Name the blood parasite species.
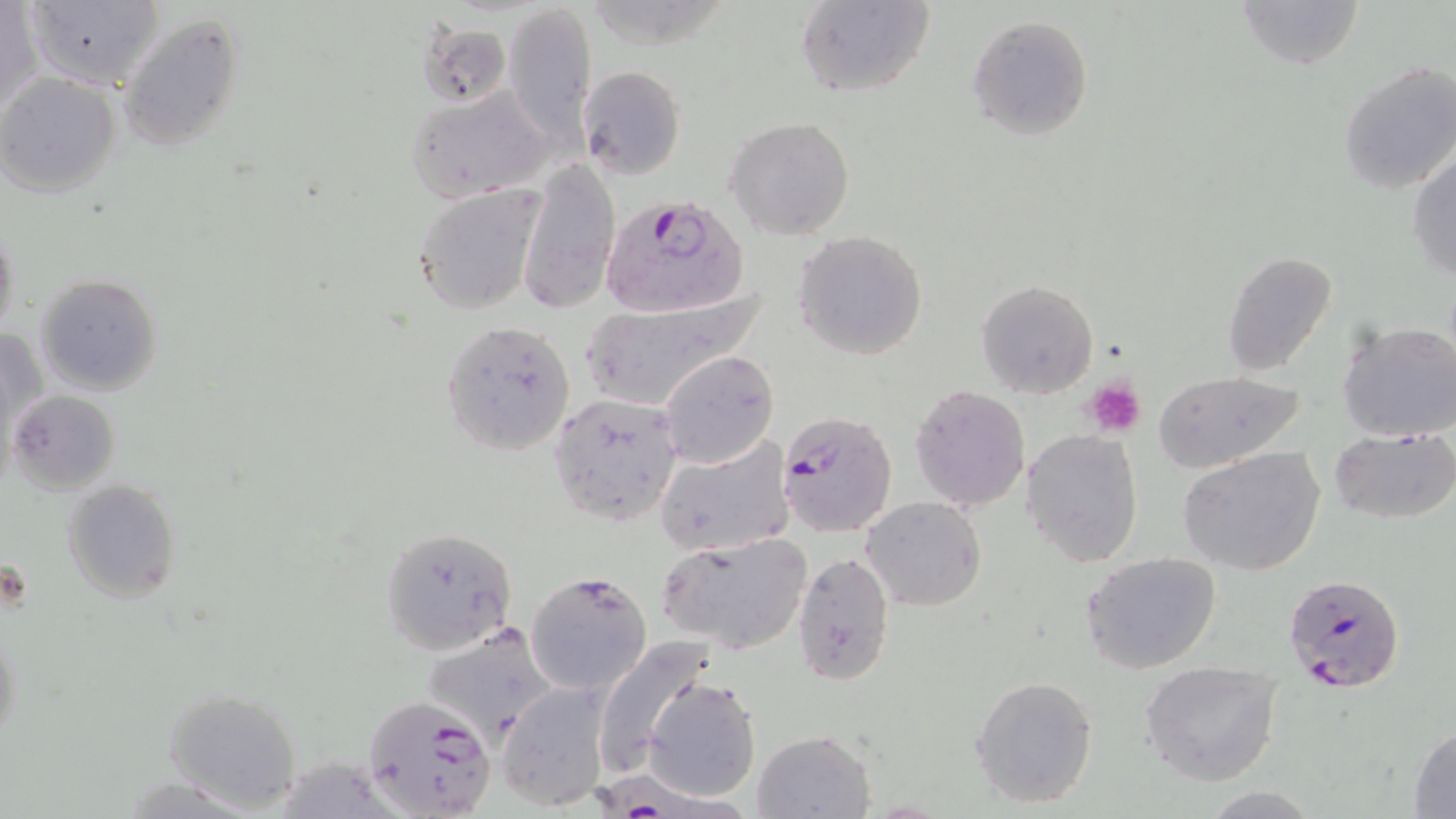
Plasmodium falciparum.

stain = May-Grünwald-Giemsa
Plasmodium falciparum-infected red blood cell locations = approximate bounding boxes as (x1, y1, x2, y2) in pixels: (601, 194, 749, 321), (775, 407, 898, 538), (1282, 572, 1405, 695), (360, 693, 499, 817), (602, 767, 752, 819)
field of view = one of a larger specimen
magnification = 1000x
image size = 1456×819 pixels
platelet locations = approximate bounding boxes as (x1, y1, x2, y2) in pixels: (1084, 378, 1146, 439)
modality = light microscopy
preparation = thin blood film
uninfected red blood cell locations = approximate bounding boxes as (x1, y1, x2, y2) in pixels: (795, 0, 937, 99), (1229, 0, 1363, 70), (1, 1, 41, 118), (23, 1, 163, 89), (503, 4, 597, 140), (117, 13, 247, 151), (967, 14, 1094, 140), (413, 16, 510, 108), (1337, 60, 1456, 195), (578, 65, 686, 178), (0, 74, 122, 196), (405, 84, 557, 203), (726, 117, 855, 239), (1408, 150, 1456, 281), (519, 157, 621, 314), (412, 185, 548, 315), (1, 220, 20, 345), (793, 231, 928, 360), (1223, 252, 1337, 376), (33, 273, 163, 396), (977, 279, 1097, 398), (576, 290, 765, 411), (440, 318, 576, 457), (1336, 319, 1456, 442), (2, 325, 47, 451), (660, 349, 779, 467), (1152, 370, 1308, 471), (909, 384, 1032, 512), (8, 389, 121, 495), (547, 391, 684, 527), (1330, 427, 1456, 524), (1020, 429, 1144, 567), (654, 436, 793, 558), (1177, 447, 1324, 576), (64, 478, 182, 605), (861, 497, 985, 610), (380, 528, 517, 655), (655, 534, 813, 655), (792, 551, 895, 683), (1081, 553, 1223, 674), (525, 570, 652, 696), (0, 627, 23, 750), (591, 635, 722, 775), (1140, 661, 1283, 786), (971, 674, 1099, 808), (644, 675, 761, 801), (164, 685, 303, 812), (498, 685, 609, 810), (1407, 724, 1456, 817), (753, 729, 876, 818)